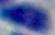
Photomicrograph. 1000x magnification. Toxoplasma gondii is shown.